State which cell type is depicted.
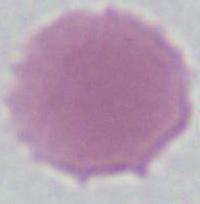

This is an erythrocyte.

Summary:
  - Magnification: 1000x
  - Modality: micrograph